Report the malaria status of this cell.
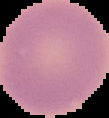
It is uninfected.

Image is 109×118 pixels. The area outside the segmented cell region is set to black. From a thin blood smear.